Locate every Plasmodium parasite.
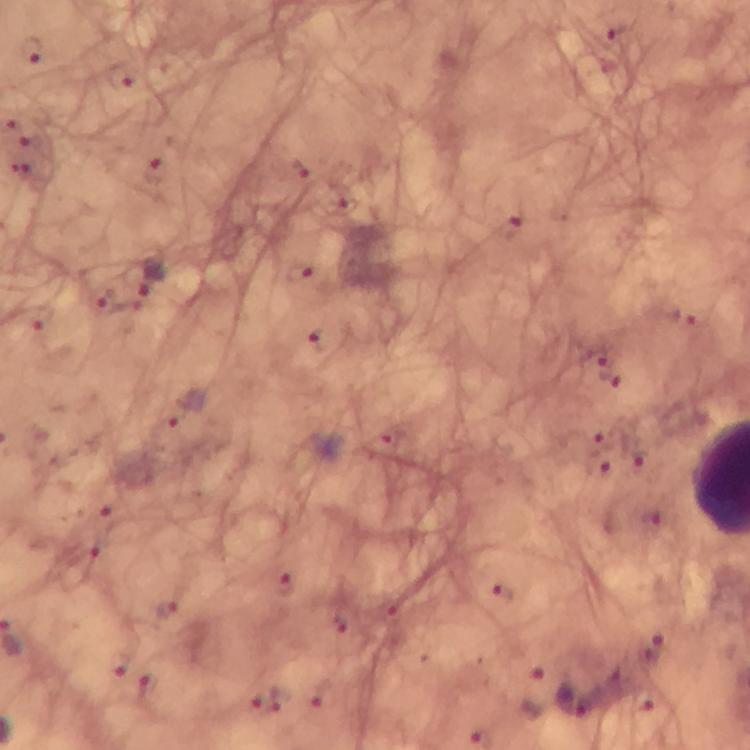
Approximate object centers, in pixels from the top-left corner.
Plasmodium parasites: (x=622, y=36), (x=122, y=78), (x=299, y=169), (x=154, y=171), (x=508, y=227), (x=301, y=273), (x=152, y=279), (x=324, y=339), (x=596, y=356), (x=609, y=379), (x=285, y=584), (x=503, y=595), (x=165, y=609), (x=654, y=651), (x=117, y=667), (x=279, y=700), (x=572, y=700).

cropped from = a single field of view
immersion oil = used
preparation = thick blood film
stain = Giemsa
magnification = 100x
image size = 750×750 pixels
context = from a diagnostic examination for malaria
capture = smartphone mounted on the microscope